Assess this cell for malaria.
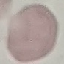

Uninfected.

capture = smartphone camera at the microscope eyepiece
stain = Giemsa
preparation = thin smear
image type = automatically extracted cell patch, resized to 64 × 64 pixels